Give the extent of all Plasmodium falciparum-infected red blood cells.
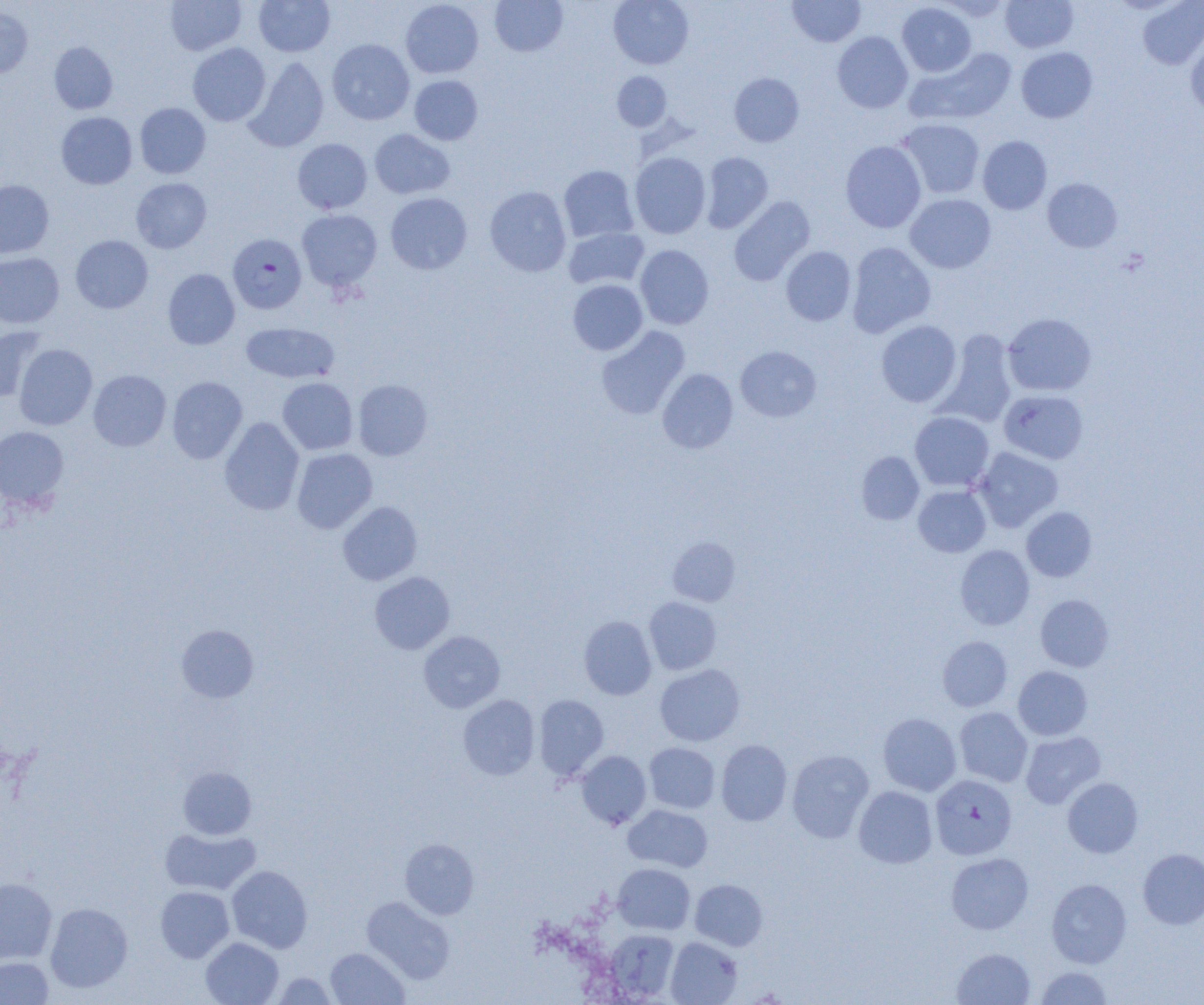

Approximate bounding boxes as [x1, y1, x2, y2] in pixels.
Plasmodium falciparum-infected red blood cells: [228, 233, 307, 313], [930, 774, 1017, 860].

Summary:
  - Uninfected red blood cell locations: [165, 0, 247, 55], [253, 0, 335, 56], [490, 0, 568, 57], [608, 0, 694, 69], [787, 0, 866, 47], [1000, 0, 1078, 52], [400, 1, 484, 78], [1138, 1, 1204, 69], [897, 2, 976, 77], [0, 6, 33, 77], [832, 31, 913, 113], [1185, 32, 1204, 117], [327, 39, 414, 125], [49, 42, 118, 114], [187, 43, 271, 126], [1016, 47, 1097, 123], [909, 48, 1017, 125], [244, 57, 329, 152], [612, 71, 671, 131], [729, 73, 804, 147], [409, 75, 483, 145], [135, 103, 211, 178], [56, 111, 137, 189], [897, 119, 985, 199], [369, 129, 455, 199], [978, 136, 1052, 215], [293, 138, 372, 214], [840, 141, 926, 233], [630, 152, 711, 238], [700, 152, 774, 233], [558, 165, 639, 243], [131, 177, 212, 253], [1042, 178, 1122, 252], [0, 180, 54, 258], [485, 186, 571, 276], [385, 192, 472, 275], [905, 194, 996, 273], [729, 196, 815, 285], [297, 209, 382, 291], [563, 227, 649, 290], [70, 235, 153, 313], [846, 242, 936, 338], [635, 245, 714, 329], [781, 246, 856, 326], [0, 252, 64, 327], [163, 269, 240, 349], [568, 279, 648, 355], [1003, 313, 1096, 396], [876, 320, 962, 407], [241, 322, 339, 383], [0, 326, 47, 402], [596, 326, 690, 419], [937, 330, 1018, 427], [14, 344, 97, 430], [735, 346, 821, 422], [657, 368, 738, 453], [88, 370, 171, 451], [167, 376, 247, 464], [277, 378, 357, 455], [353, 379, 432, 461], [999, 389, 1088, 464], [910, 411, 994, 491], [219, 417, 304, 515], [0, 425, 69, 509], [973, 447, 1063, 532], [292, 448, 377, 533], [856, 451, 924, 524], [913, 485, 991, 557], [337, 500, 423, 585], [1021, 507, 1097, 582], [668, 537, 741, 605], [955, 545, 1035, 630], [369, 571, 455, 654], [1035, 594, 1114, 672], [644, 597, 721, 674], [579, 616, 657, 700], [176, 624, 258, 702], [418, 630, 505, 713], [938, 636, 1012, 711], [655, 664, 745, 746], [1013, 666, 1092, 740], [533, 694, 609, 780], [458, 695, 540, 780], [954, 707, 1032, 787], [878, 712, 961, 796], [1020, 731, 1106, 808], [716, 740, 792, 826], [644, 742, 720, 814], [787, 749, 874, 842], [576, 751, 651, 829], [178, 766, 257, 839], [1062, 777, 1143, 858], [853, 786, 937, 868], [622, 804, 712, 872], [160, 827, 261, 895], [400, 838, 479, 919], [1138, 848, 1204, 929], [946, 852, 1034, 934], [612, 863, 695, 934], [227, 865, 312, 953], [0, 877, 57, 964], [690, 878, 768, 950], [1046, 878, 1131, 968], [155, 886, 234, 962], [361, 895, 456, 984], [45, 902, 133, 993], [604, 929, 679, 1001], [201, 937, 283, 1005], [665, 937, 742, 1005], [325, 948, 409, 1005], [952, 948, 1035, 1005], [0, 957, 53, 1004], [1035, 966, 1113, 1005], [272, 972, 337, 1004]
  - Slide-level diagnosis: Plasmodium falciparum
  - Field of view: one of a larger specimen
  - Modality: light microscopy
  - Magnification: 1000x
  - Preparation: thin blood smear
  - Image size: 1204×1005 pixels